Assess this cell for malaria.
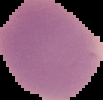

It is uninfected.

Image is 103×100 pixels. From a thin blood smear. Segmented cell region on a black background.